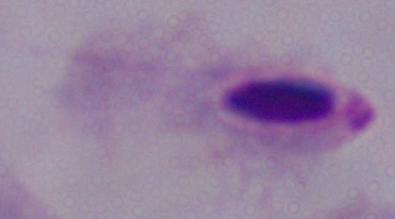
identification = trichomonad
magnification = 1000x
modality = micrograph